Classify this cell by malaria status.
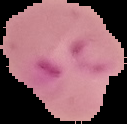

Parasitized.

Image is 127×124 pixels. From a thin blood smear. Cell region segmented out of the field of view; the surrounding area is masked to black.